Identify the preparation type.
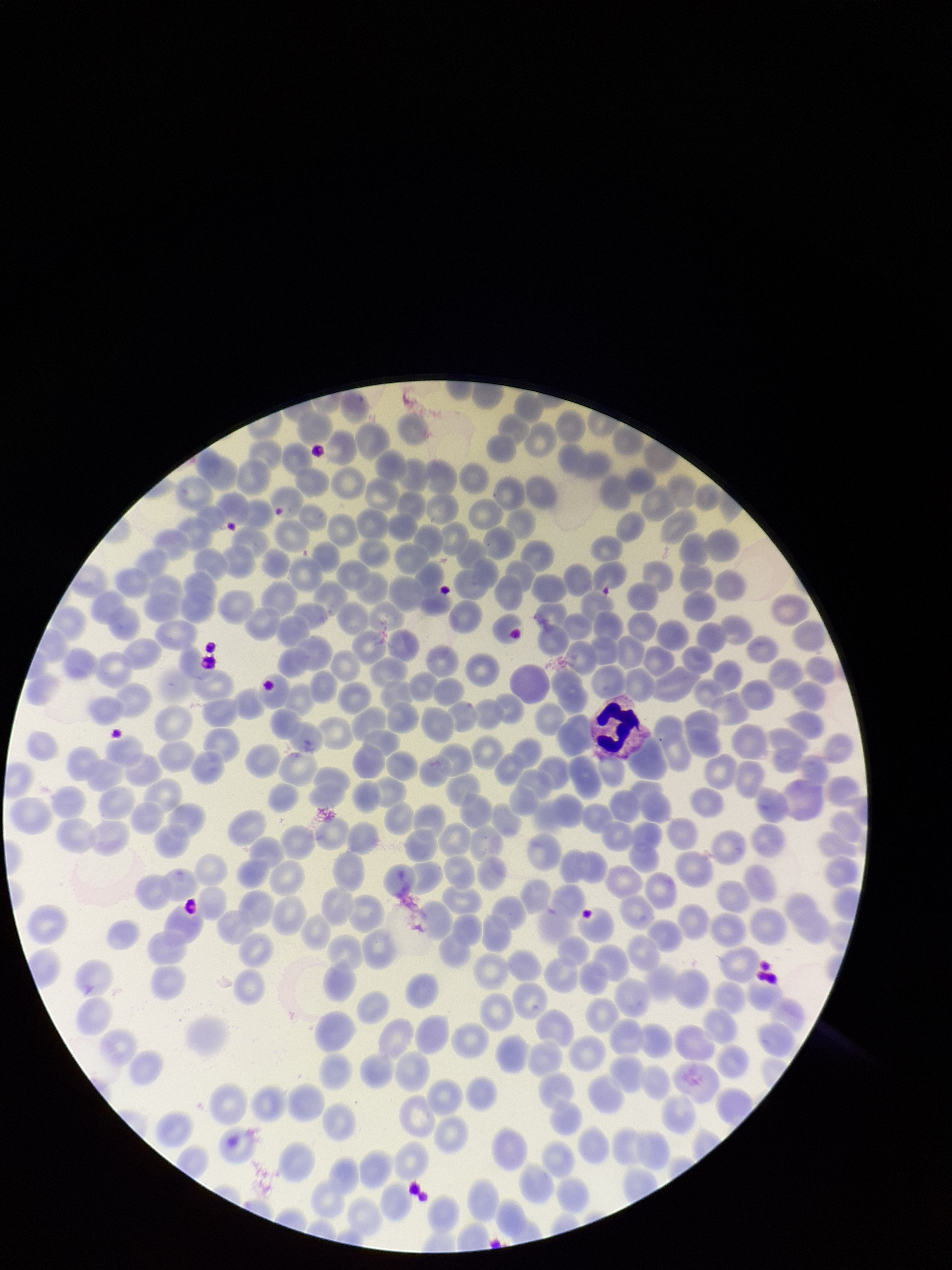

A thin smear.

Parasitized red blood cell count: 0. Stained with Giemsa. Red blood cell count: 300. Patient malaria status: infected. Species reported for this patient: Plasmodium vivax. Smartphone photograph taken through the eyepiece of a microscope. Parasitized red blood cells: none seen. One field from this slide. Image is 952×1270 pixels.